State which cell type is depicted.
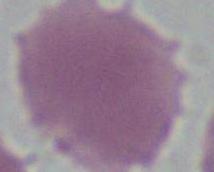
An erythrocyte.

modality = micrograph
magnification = 1000x